Locate every Plasmodium parasite.
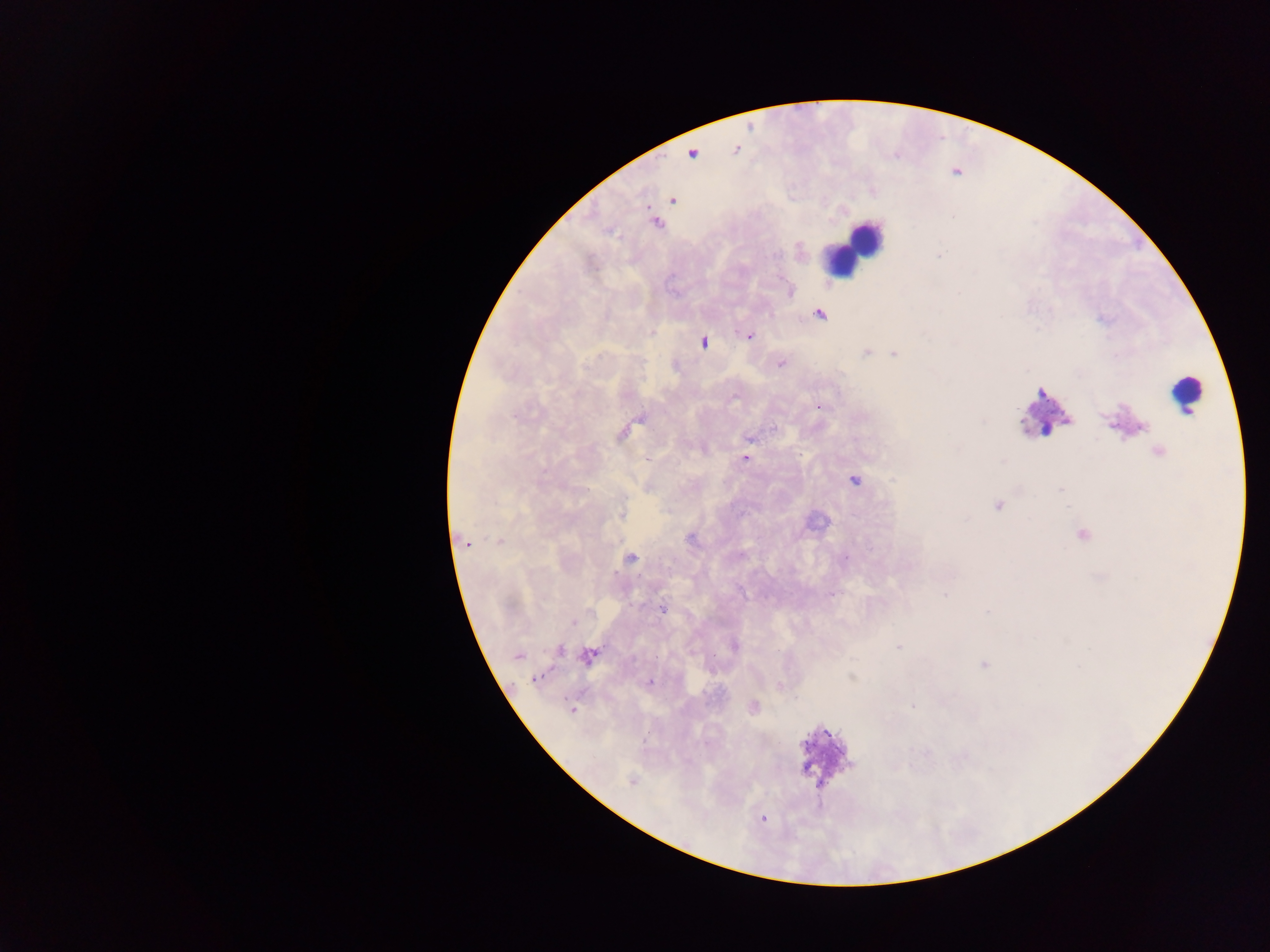

Approximate centers as {x, y} in pixels.
Plasmodium parasites: {692, 154}, {673, 200}, {953, 216}, {656, 223}, {938, 255}, {790, 292}, {820, 315}, {748, 335}, {704, 342}, {866, 352}, {894, 353}, {780, 365}, {819, 406}, {1113, 424}, {774, 429}, {623, 434}, {748, 439}, {1159, 452}, {744, 458}, {646, 459}, {854, 481}, {1060, 489}, {997, 506}, {621, 514}, {1083, 534}, {691, 539}, {500, 541}, {464, 543}, {844, 558}, {632, 559}, {831, 594}, {944, 595}, {662, 608}, {589, 611}, {986, 612}, {574, 622}, {734, 647}, {899, 648}, {559, 650}, {518, 655}, {589, 655}, {983, 664}, {851, 677}, {537, 678}, {650, 682}, {779, 685}, {912, 706}, {753, 707}, {571, 710}, {631, 780}, {763, 819}.

{
  "capture": "mobile-phone photograph through a microscope",
  "field_of_view": "single",
  "leukocyte_locations": "approximate centers as {x, y} in pixels: {861, 240}, {843, 256}, {1186, 393}, {1042, 406}",
  "country": "Ghana",
  "preparation": "thick blood film",
  "image_size": "1270×952 pixels"
}